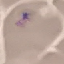
Result: malaria parasites identified. Automatically extracted cell patch, resized to 64 × 64 pixels. Thin blood smear. Photographed with a smartphone camera at the microscope eyepiece. Giemsa stain.